State which parasite is depicted.
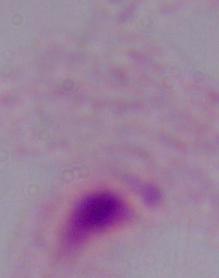
This is a trichomonad.

Summary:
  - Modality: photomicrograph
  - Magnification: 1000x